Report the malaria status of this cell.
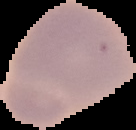

It is uninfected.

Summary:
  - Preparation: thin blood film
  - Image type: segmented cell region with the area outside set to black
  - Image size: 136×130 pixels